Describe the morphology of the red blood cells.
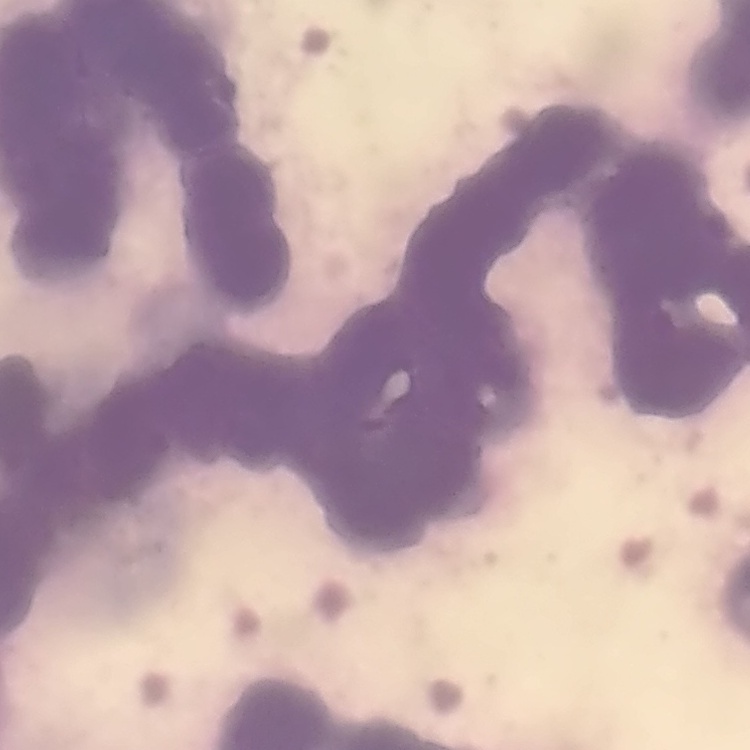

Rouleaux formation.

Summary:
  - Image type: one tile cut from a larger photomicrograph
  - Preparation: thin blood smear
  - Stain: Field's or Giemsa